Point out each malaria parasite.
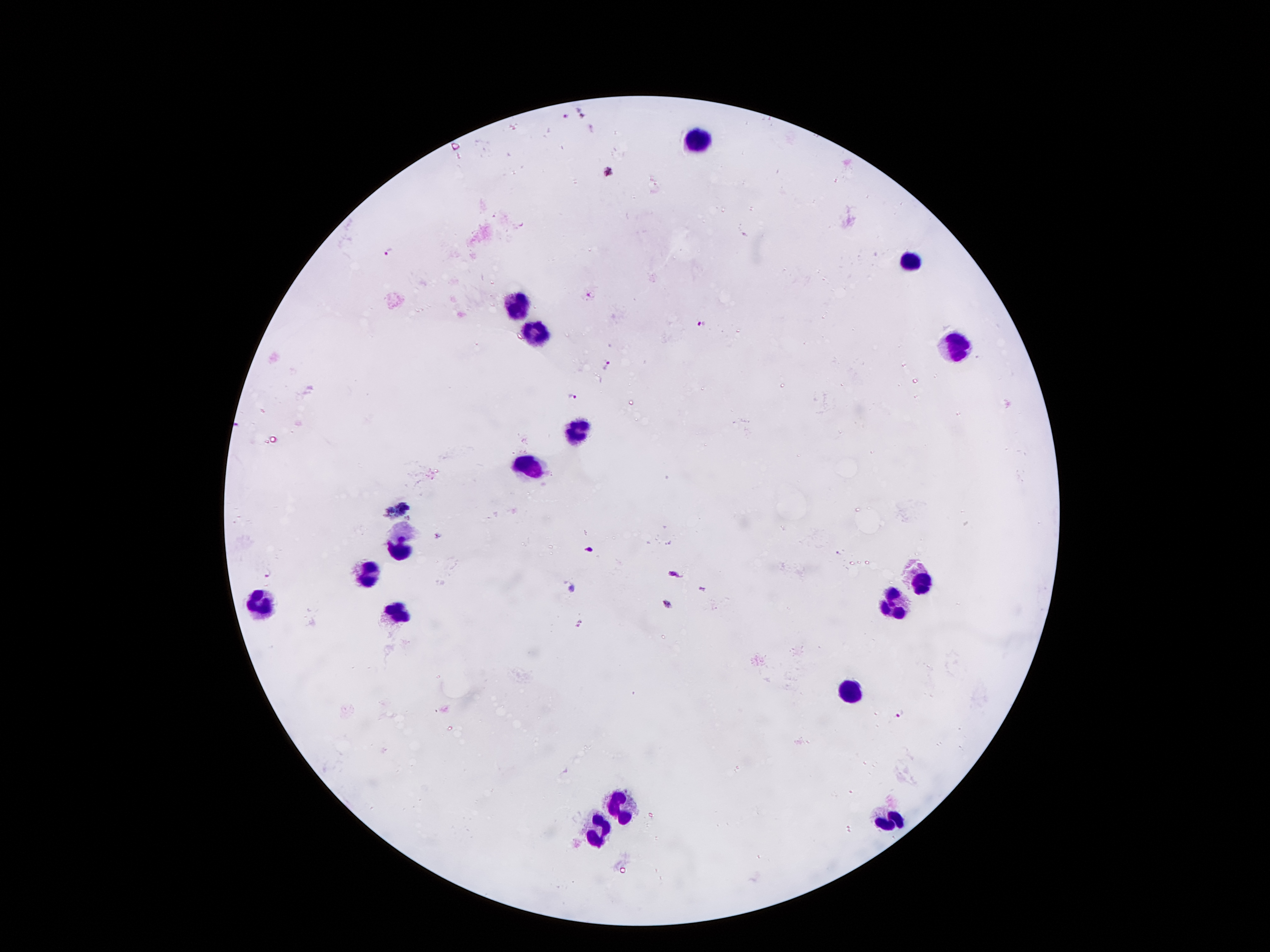

Approximate centers as (x, y) in pixels.
Malaria parasites: (584, 113), (564, 116), (389, 251), (589, 295), (702, 324), (607, 363), (572, 396), (437, 535), (588, 549), (268, 572), (675, 575), (573, 589), (667, 604), (580, 624), (901, 713).

Summary:
  - Leukocyte locations: (696, 137), (911, 261), (513, 303), (536, 333), (953, 345), (573, 431), (526, 464), (400, 546), (369, 572), (922, 582), (261, 601), (899, 609), (402, 611), (853, 693), (621, 805), (889, 819), (599, 831)
  - Preparation: thick peripheral-blood smear
  - Capture: smartphone through the microscope eyepiece
  - Magnification: 100x
  - Patient malaria status: infected with Plasmodium falciparum
  - Field of view: one from this slide
  - Stain: Giemsa
  - Image size: 1270×952 pixels